State the preparation type.
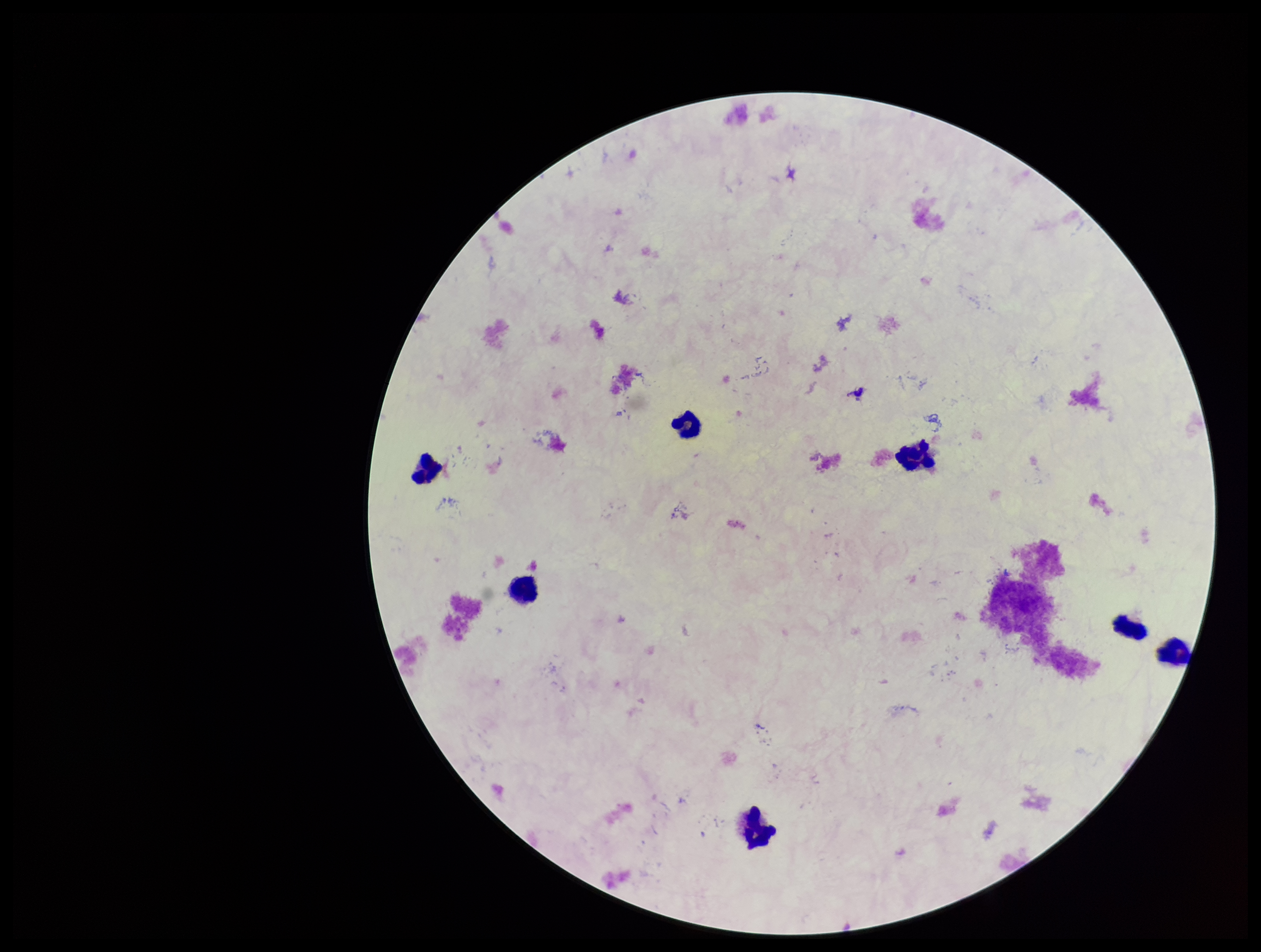

Thick.

leukocyte_count: 7
field_of_view: single
parasite_count: 0
stain: Giemsa
image_size: 1261×952 pixels
patient_malaria_status: negative
plasmodium_parasites: none identified
capture: smartphone photograph through the microscope eyepiece